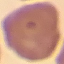 Result: negative for malaria parasites. Automatically extracted cell patch, resized to 64 × 64 pixels. Thin blood film. Giemsa-stained preparation. Photographed with a smartphone camera at the microscope eyepiece.